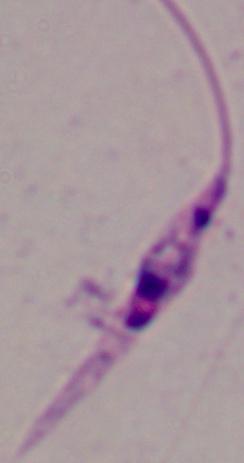

identification = Leishmania
magnification = 1000x
modality = micrograph